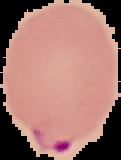

image size = 121×160 pixels
image type = segmented cell region with the area outside set to black
preparation = thin blood smear
malaria status = parasitized